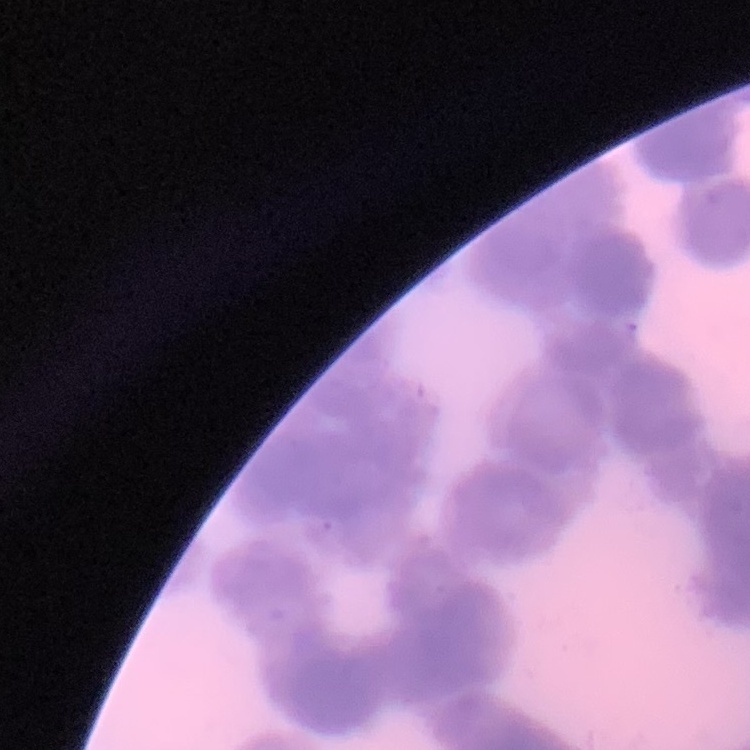

Summary:
  - Erythrocyte morphology: rouleaux formation
  - Stain: Field's or Giemsa
  - Preparation: thin peripheral smear
  - Image type: one tile cut from a larger photomicrograph